Locate the red blood cells and classify each one as Plasmodium falciparum-infected, uninfected, or of indeterminate infection status.
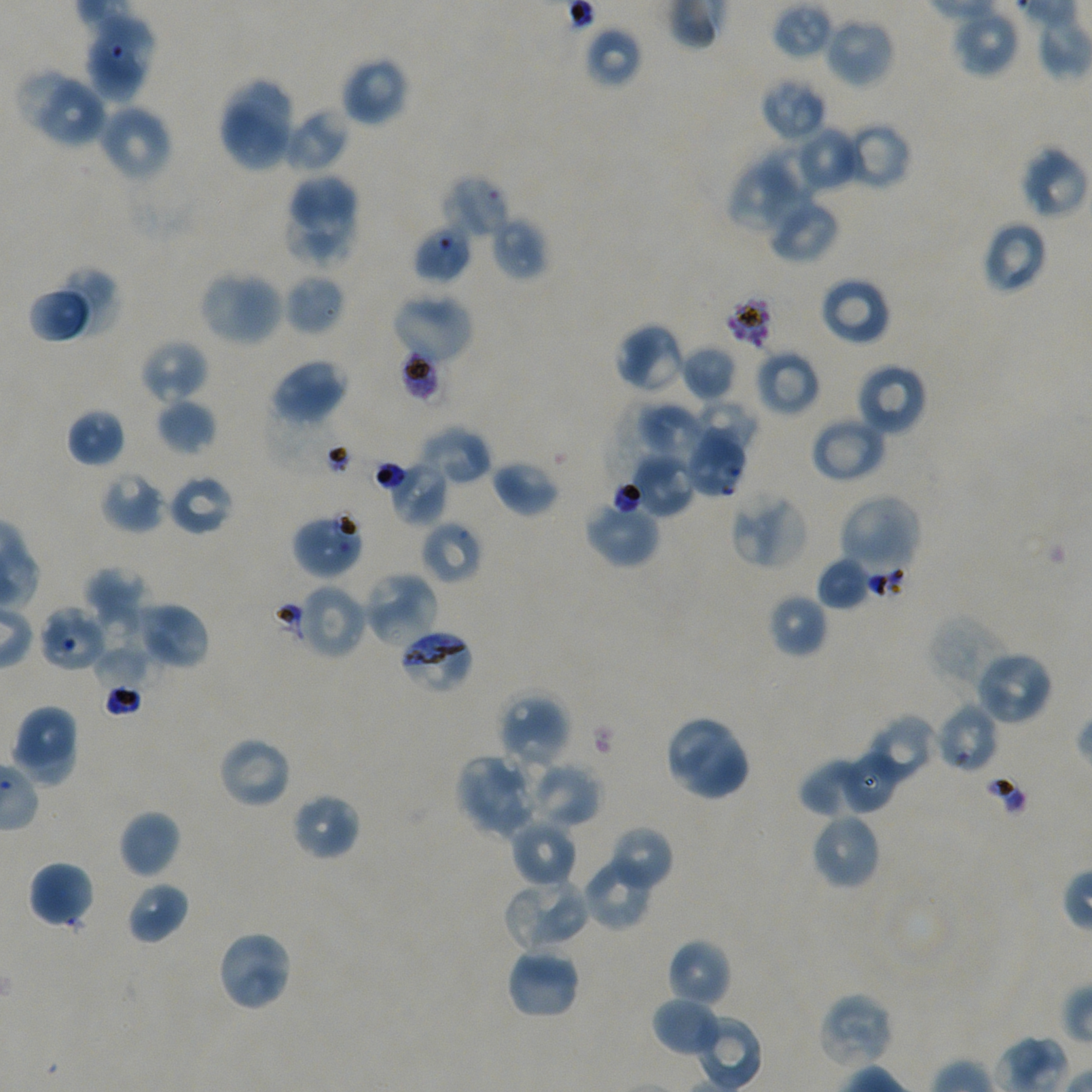
Approximate bounding boxes as (x1, y1, x2, y2) in pixels. Not every red blood cell is marked.
Infected red blood cells: (398, 627, 475, 695).
Red blood cells of indeterminate infection status: (412, 225, 471, 283), (405, 350, 452, 407), (382, 459, 448, 526), (295, 583, 368, 660), (934, 702, 998, 774).
Uninfected red blood cells: (772, 1, 835, 60), (951, 7, 1019, 78), (84, 12, 157, 105), (823, 16, 896, 89), (584, 26, 642, 89), (340, 55, 410, 127), (217, 77, 297, 172), (760, 77, 826, 143), (38, 81, 109, 149), (96, 104, 173, 182), (281, 106, 351, 174), (839, 122, 911, 191), (791, 125, 862, 192), (1019, 147, 1089, 220), (727, 155, 812, 234), (282, 173, 359, 235), (443, 175, 510, 241), (765, 194, 839, 264), (283, 209, 358, 272), (489, 214, 549, 280), (981, 221, 1049, 295), (59, 267, 118, 334), (198, 269, 285, 347), (284, 273, 346, 336), (819, 276, 892, 346), (390, 291, 475, 365), (28, 293, 90, 341), (614, 322, 687, 394), (139, 339, 208, 404), (680, 344, 739, 402), (754, 348, 820, 417), (270, 359, 348, 426), (854, 362, 927, 437), (156, 397, 217, 455), (695, 399, 760, 456), (636, 403, 710, 469), (66, 407, 126, 468), (809, 416, 887, 484), (685, 423, 748, 498), (418, 424, 492, 486), (625, 452, 697, 518), (490, 459, 560, 517), (101, 471, 164, 533), (167, 473, 235, 536), (729, 491, 809, 570), (837, 493, 921, 574), (584, 499, 661, 568), (291, 511, 364, 579), (420, 520, 483, 585), (816, 556, 873, 611), (84, 567, 148, 627), (362, 570, 439, 650), (767, 592, 829, 659), (135, 602, 210, 670), (38, 605, 108, 672), (93, 610, 148, 673), (927, 613, 1011, 693), (94, 647, 156, 696), (973, 649, 1054, 727), (496, 693, 571, 771), (10, 704, 77, 765), (663, 714, 752, 802), (866, 714, 939, 784), (11, 729, 79, 785), (217, 735, 293, 809), (839, 751, 901, 812), (456, 753, 540, 839), (526, 761, 602, 828), (799, 761, 877, 818), (291, 792, 361, 861), (118, 809, 181, 879), (809, 812, 881, 890), (510, 818, 577, 888), (606, 825, 674, 892), (581, 857, 657, 930), (28, 860, 94, 928), (503, 877, 592, 953), (126, 881, 189, 945), (216, 928, 294, 1013), (666, 938, 732, 1009), (505, 947, 581, 1021), (818, 991, 895, 1071), (651, 998, 721, 1057).

Summary:
  - Image size: 1092×1092 pixels
  - Stain: Giemsa
  - Field of view: one from this slide
  - Preparation: thin blood smear
  - Donor blood group: A+/O+
  - Culture: in-vitro Plasmodium falciparum strain NF54, static
  - Objective: 100x, oil immersion, numerical aperture 1.45